Assess the morphology of the erythrocytes.
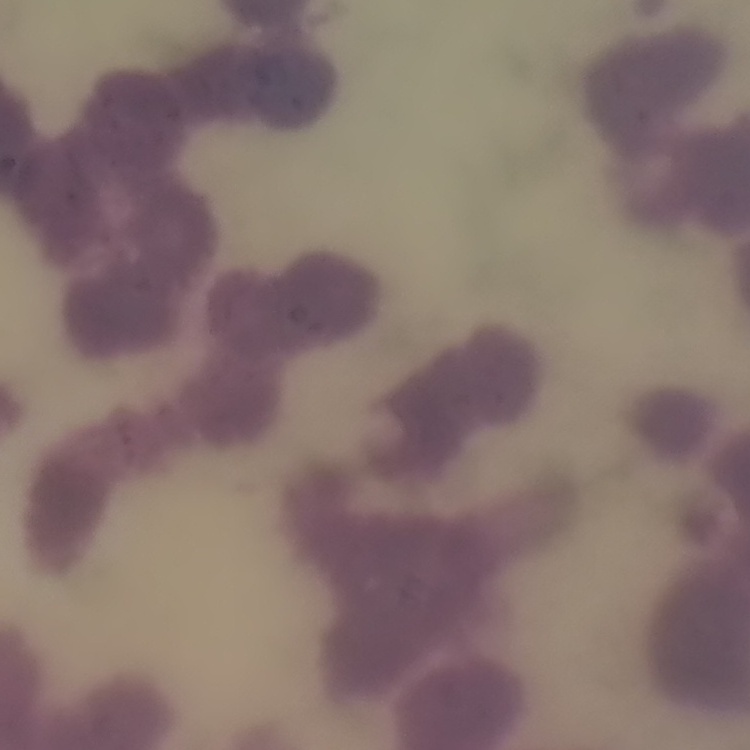
They show rouleaux formation.

Thin blood film. Field's or Giemsa stain. One tile cut from a larger photomicrograph.